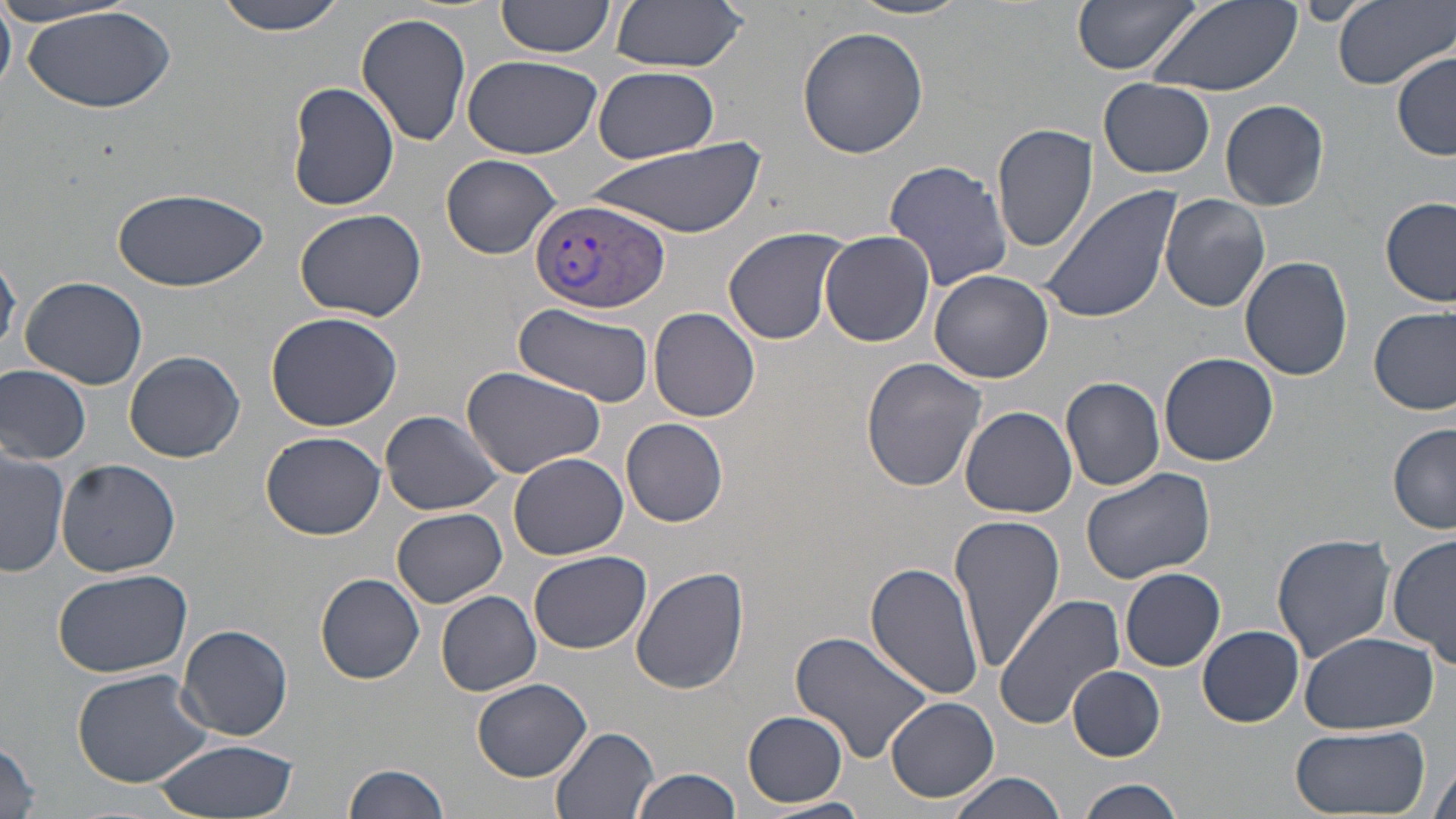

Approximate bounding boxes as named x1/y1/x2/y2 corners in pixels. Plasmodium vivax-infected red blood cell locations: (x1=529, y1=197, x2=670, y2=316). Uninfected red blood cell locations: (x1=215, y1=0, x2=346, y2=37), (x1=610, y1=0, x2=748, y2=72), (x1=843, y1=0, x2=975, y2=20), (x1=1074, y1=0, x2=1203, y2=76), (x1=1148, y1=0, x2=1301, y2=97), (x1=1332, y1=0, x2=1453, y2=90), (x1=492, y1=1, x2=617, y2=63), (x1=1296, y1=1, x2=1374, y2=26), (x1=0, y1=3, x2=16, y2=94), (x1=19, y1=4, x2=176, y2=112), (x1=357, y1=13, x2=473, y2=147), (x1=798, y1=27, x2=930, y2=156), (x1=1392, y1=51, x2=1454, y2=161), (x1=461, y1=55, x2=602, y2=160), (x1=593, y1=66, x2=717, y2=161), (x1=1100, y1=79, x2=1216, y2=178), (x1=285, y1=82, x2=398, y2=212), (x1=1220, y1=98, x2=1330, y2=211), (x1=991, y1=123, x2=1098, y2=254), (x1=589, y1=140, x2=764, y2=239), (x1=441, y1=153, x2=562, y2=259), (x1=883, y1=160, x2=1014, y2=289), (x1=1037, y1=183, x2=1181, y2=326), (x1=114, y1=186, x2=266, y2=292), (x1=1161, y1=190, x2=1271, y2=312), (x1=1381, y1=196, x2=1456, y2=308), (x1=294, y1=208, x2=428, y2=321), (x1=280, y1=212, x2=419, y2=429), (x1=723, y1=227, x2=848, y2=345), (x1=818, y1=231, x2=936, y2=348), (x1=0, y1=248, x2=21, y2=358), (x1=1240, y1=255, x2=1354, y2=381), (x1=930, y1=269, x2=1054, y2=383), (x1=20, y1=275, x2=148, y2=388), (x1=514, y1=304, x2=654, y2=409), (x1=1370, y1=306, x2=1456, y2=415), (x1=649, y1=307, x2=761, y2=423), (x1=264, y1=311, x2=403, y2=430), (x1=123, y1=350, x2=244, y2=463), (x1=1159, y1=353, x2=1279, y2=466), (x1=861, y1=357, x2=987, y2=492), (x1=0, y1=364, x2=93, y2=464), (x1=461, y1=365, x2=606, y2=475), (x1=1060, y1=375, x2=1165, y2=492), (x1=960, y1=405, x2=1077, y2=517), (x1=381, y1=409, x2=508, y2=516), (x1=621, y1=418, x2=729, y2=527), (x1=1389, y1=423, x2=1456, y2=533), (x1=260, y1=430, x2=386, y2=540), (x1=2, y1=448, x2=70, y2=576), (x1=509, y1=451, x2=628, y2=560), (x1=55, y1=460, x2=181, y2=577), (x1=1080, y1=467, x2=1217, y2=584), (x1=391, y1=507, x2=507, y2=607), (x1=951, y1=513, x2=1067, y2=672), (x1=1389, y1=532, x2=1456, y2=665), (x1=1272, y1=534, x2=1395, y2=662), (x1=528, y1=550, x2=651, y2=653), (x1=865, y1=562, x2=985, y2=703), (x1=630, y1=566, x2=751, y2=696), (x1=1120, y1=566, x2=1226, y2=672), (x1=52, y1=568, x2=195, y2=679), (x1=315, y1=573, x2=425, y2=683), (x1=436, y1=590, x2=541, y2=696), (x1=993, y1=595, x2=1124, y2=730), (x1=178, y1=624, x2=293, y2=741), (x1=1197, y1=625, x2=1304, y2=727), (x1=789, y1=629, x2=938, y2=765), (x1=1300, y1=631, x2=1437, y2=735), (x1=1067, y1=666, x2=1165, y2=762), (x1=72, y1=667, x2=214, y2=787), (x1=473, y1=678, x2=592, y2=780), (x1=884, y1=697, x2=1000, y2=804), (x1=743, y1=711, x2=849, y2=808), (x1=1285, y1=723, x2=1429, y2=816), (x1=550, y1=724, x2=661, y2=819), (x1=0, y1=737, x2=43, y2=819), (x1=152, y1=739, x2=298, y2=818), (x1=1429, y1=761, x2=1455, y2=819), (x1=344, y1=762, x2=452, y2=819), (x1=632, y1=768, x2=742, y2=819), (x1=946, y1=774, x2=1071, y2=819), (x1=1074, y1=778, x2=1186, y2=819), (x1=756, y1=798, x2=872, y2=818). Slide-level diagnosis: Plasmodium vivax. Captured at 1000x magnification. Thin blood film. Optical microscopy. One field of a larger specimen. Image is 1456×819 pixels. May-Grünwald-Giemsa stain.